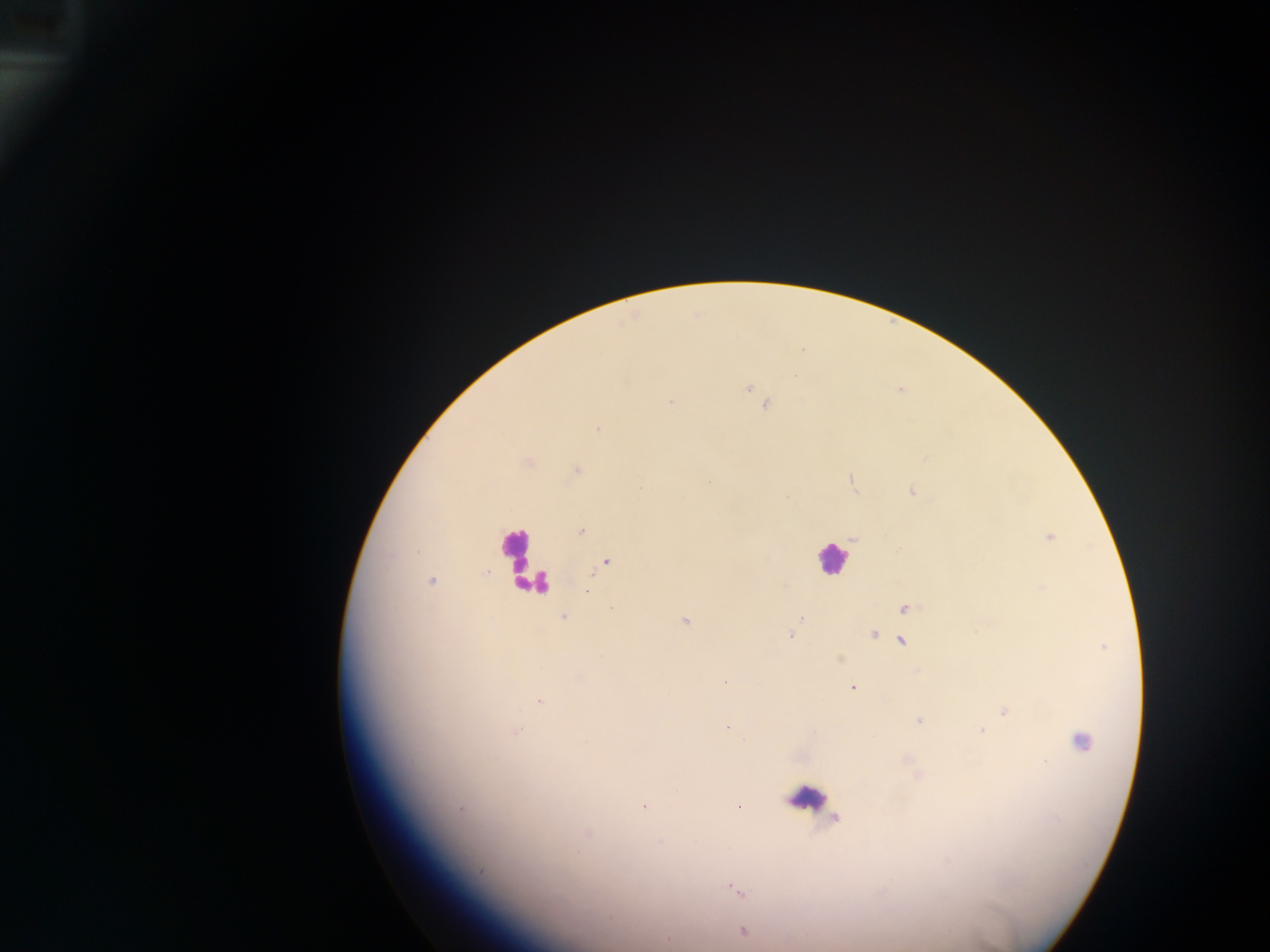

{
  "image_size": "1270×952 pixels",
  "field_of_view": "single",
  "malaria_parasite_locations": "approximate centers as {x, y} in pixels: {796, 378}, {748, 388}, {671, 402}, {764, 403}, {597, 427}, {926, 457}, {577, 469}, {910, 491}, {580, 531}, {1051, 536}, {607, 562}, {601, 567}, {485, 574}, {590, 576}, {433, 580}, {588, 585}, {785, 587}, {586, 592}, {612, 609}, {903, 609}, {562, 616}, {800, 618}, {685, 621}, {873, 634}, {789, 636}, {900, 641}, {839, 659}, {579, 678}, {724, 681}, {852, 687}, {538, 702}, {1005, 711}, {916, 720}, {726, 725}, {980, 730}, {515, 733}, {1076, 741}, {644, 805}, {738, 806}, {462, 808}, {837, 817}, {589, 833}, {947, 860}, {480, 870}, {727, 886}, {734, 890}, {741, 892}, {741, 931}",
  "capture": "mobile-phone photograph through a microscope",
  "country": "Ghana",
  "preparation": "thick blood smear",
  "leukocyte_locations": "approximate centers as {x, y} in pixels: {514, 549}, {832, 566}, {802, 797}"
}